Draw a bounding box around every leukocyte (white blood cell).
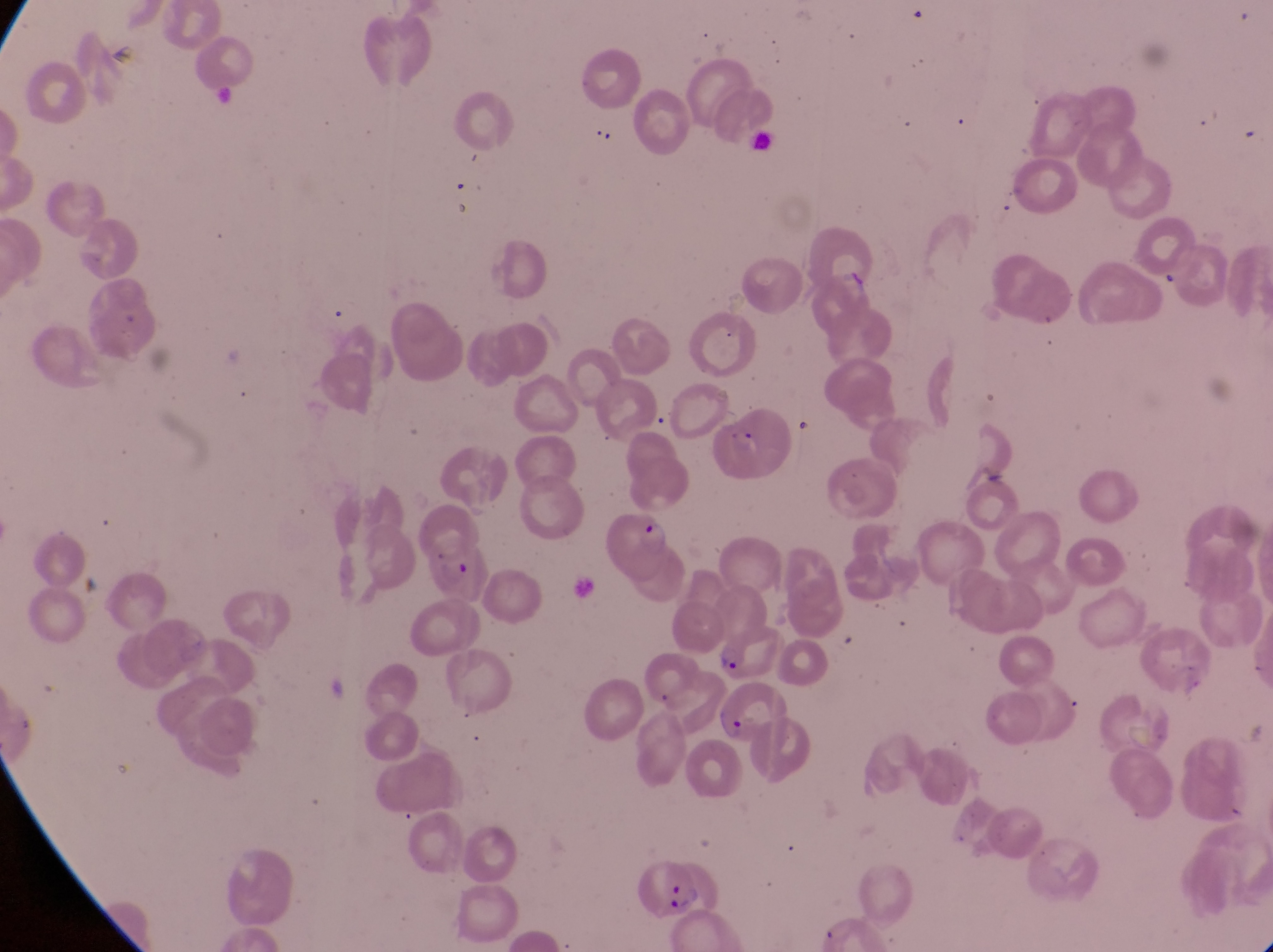

No leukocytes observed.

preparation = thin blood film
field of view = single
country = Uganda
capture = smartphone photograph through the eyepiece of an Olympus CX-23 microscope
magnification = 1000x
parasitised red blood cell locations = approximate bounding boxes as {left, top, right, bottom} in pixels: {601, 509, 675, 589}, {426, 545, 493, 608}, {717, 681, 791, 751}, {634, 849, 721, 917}
trophozoite locations = approximate bounding boxes as {left, top, right, bottom} in pixels: {714, 642, 751, 682}
image size = 1273×952 pixels